Identify the parasite.
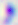

This is Toxoplasma gondii.

modality = photomicrograph
magnification = 400x